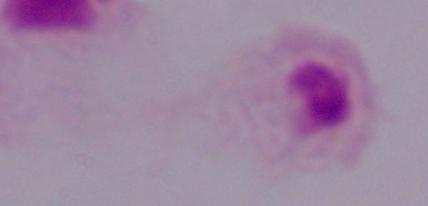
modality = photomicrograph
identification = trichomonad
magnification = 1000x